Report the malaria status of this cell.
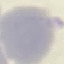
Uninfected.

Summary:
  - Capture: smartphone through the microscope eyepiece
  - Stain: Giemsa
  - Image type: cell patch, automatically extracted from a larger field of view and resized to 64 × 64 pixels
  - Preparation: thin blood smear